Point out each malaria parasite.
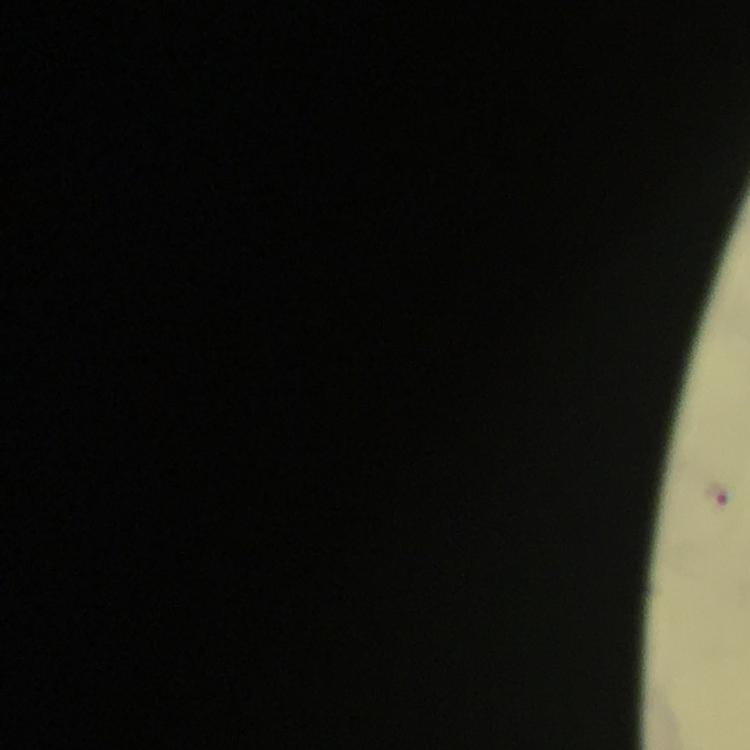

Approximate object centers, in pixels from the top-left corner.
Malaria parasites: (x=716, y=494).

Summary:
  - Capture: smartphone camera through the microscope
  - Stain: Giemsa
  - Context: from a malaria diagnostic workup
  - Cropped from: one field of view
  - Magnification: 100x
  - Image size: 750×750 pixels
  - Immersion oil: used
  - Preparation: thick blood film